Outline each uninfected red blood cell.
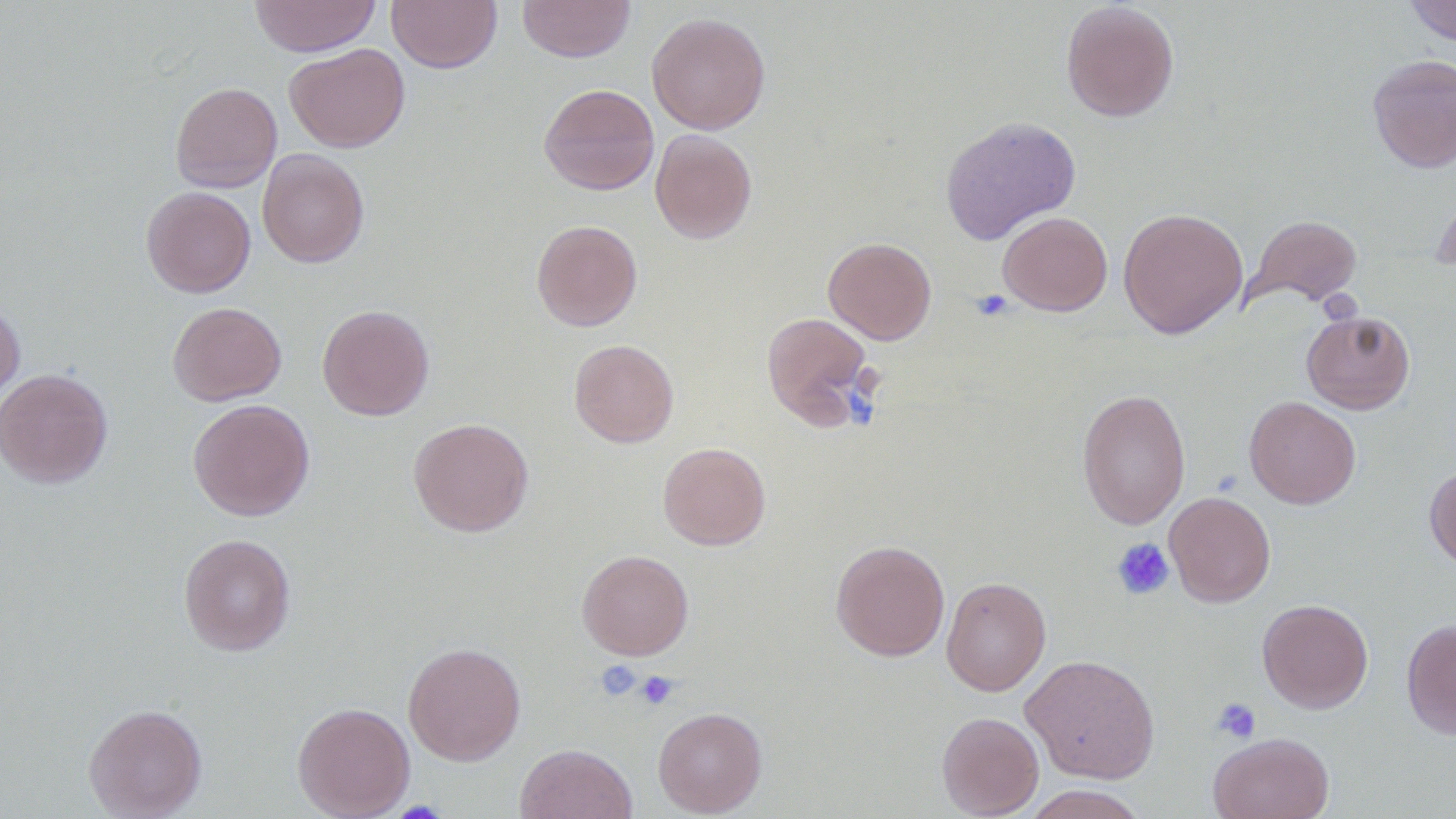

Approximate bounding boxes as (x1, y1, x2, y2) in pixels.
Uninfected red blood cells: (248, 0, 381, 57), (386, 0, 502, 73), (518, 0, 635, 62), (1404, 0, 1456, 46), (1060, 1, 1180, 122), (646, 12, 771, 134), (284, 43, 410, 153), (1367, 54, 1456, 173), (170, 81, 282, 193), (539, 83, 659, 195), (940, 115, 1081, 245), (650, 129, 757, 244), (257, 148, 369, 267), (1430, 185, 1456, 275), (141, 186, 256, 297), (1118, 207, 1248, 339), (997, 211, 1112, 316), (1247, 215, 1362, 307), (531, 220, 642, 331), (823, 237, 936, 344), (0, 300, 25, 408), (168, 302, 286, 406), (317, 304, 434, 421), (1301, 309, 1415, 414), (761, 311, 874, 428), (569, 340, 679, 447), (0, 368, 113, 488), (1077, 388, 1191, 529), (1244, 395, 1361, 509), (187, 399, 315, 521), (408, 417, 534, 536), (658, 442, 771, 550), (1424, 465, 1456, 571), (1164, 491, 1276, 607), (178, 533, 296, 656), (830, 539, 950, 661), (577, 550, 694, 660), (941, 577, 1050, 696), (1257, 598, 1374, 713), (1401, 618, 1456, 738), (403, 642, 526, 764), (1021, 653, 1160, 783), (292, 701, 415, 819), (84, 703, 207, 818), (653, 706, 767, 817), (937, 711, 1044, 818), (1208, 732, 1334, 819), (515, 742, 636, 819), (1020, 785, 1149, 819).

Platelet locations: (970, 289, 1014, 321), (849, 391, 874, 426), (1112, 537, 1175, 600), (594, 660, 642, 702), (634, 670, 679, 710), (1211, 697, 1262, 744). Slide-level diagnosis: no evidence of blood parasites. Thin blood film. One field of a larger specimen. Image is 1456×819 pixels. Optical microscopy. Captured at 1000x magnification.